Give the extent of all Babesia divergens-infected red blood cells.
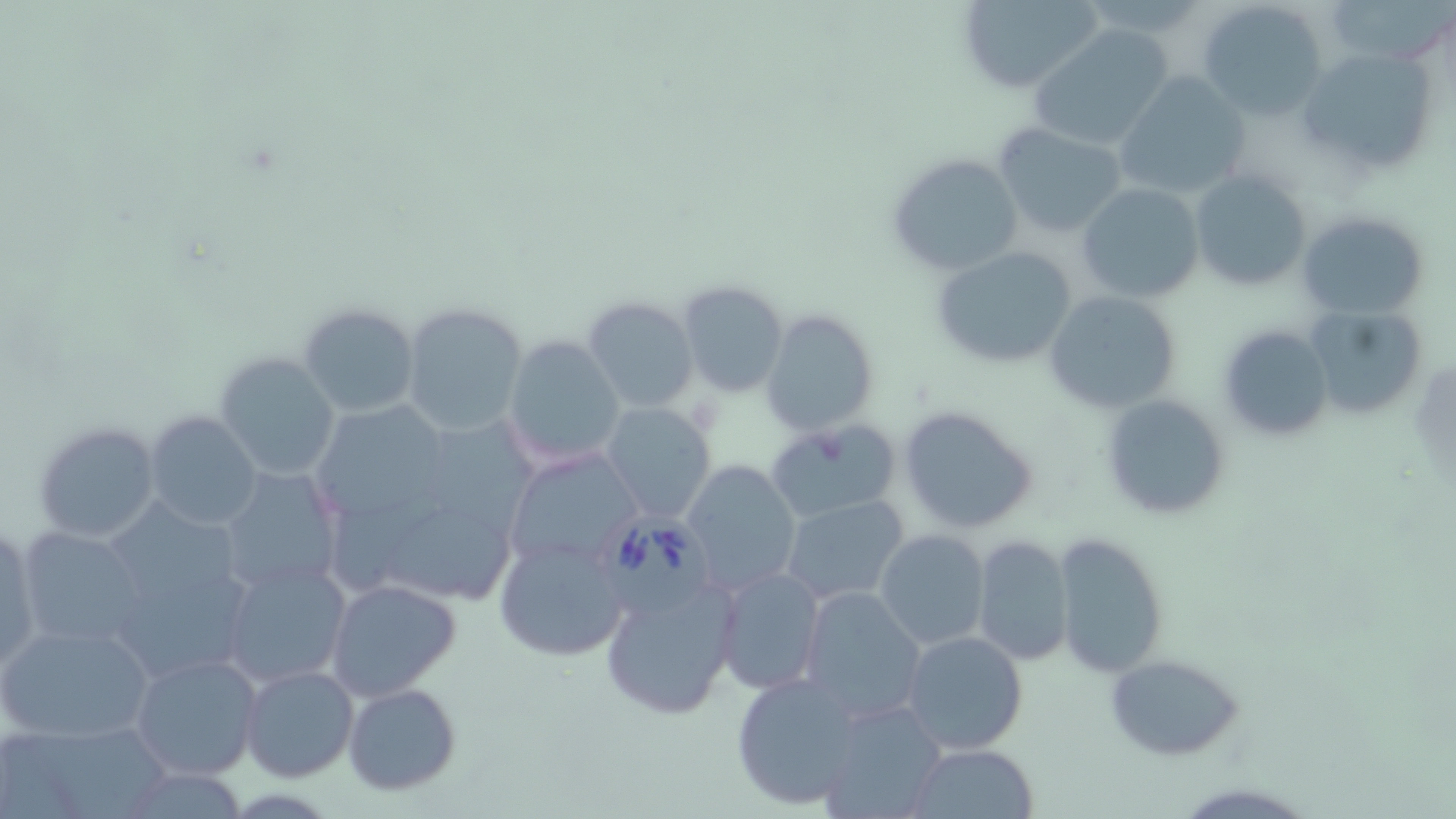
Approximate bounding boxes as [x1, y1, x2, y2] in pixels.
Babesia divergens-infected red blood cells: [604, 513, 716, 625].

Uninfected red blood cell locations: [956, 0, 1105, 94], [1328, 0, 1454, 64], [1196, 1, 1328, 120], [1027, 25, 1176, 150], [1299, 44, 1440, 176], [1113, 71, 1252, 202], [992, 121, 1130, 238], [888, 151, 1025, 275], [1191, 169, 1313, 292], [1077, 184, 1205, 302], [1298, 210, 1429, 317], [930, 244, 1077, 369], [677, 279, 789, 398], [1042, 288, 1181, 415], [581, 295, 698, 414], [400, 301, 529, 437], [295, 302, 419, 419], [1306, 305, 1429, 420], [761, 308, 879, 436], [1216, 323, 1334, 441], [504, 335, 626, 470], [215, 352, 342, 482], [1099, 393, 1230, 522], [305, 399, 456, 527], [600, 402, 717, 523], [898, 404, 1041, 535], [145, 411, 263, 530], [432, 414, 543, 531], [764, 418, 901, 524], [33, 420, 162, 544], [503, 448, 640, 572], [682, 457, 801, 595], [216, 465, 345, 597], [699, 471, 817, 681], [334, 492, 449, 597], [778, 494, 911, 606], [390, 515, 526, 607], [106, 518, 255, 689], [16, 526, 150, 655], [0, 527, 42, 674], [875, 530, 990, 650], [1051, 531, 1170, 678], [495, 535, 630, 663], [972, 535, 1074, 667], [218, 559, 352, 688], [712, 566, 827, 696], [601, 576, 738, 720], [325, 578, 460, 700], [797, 586, 925, 724], [799, 606, 1029, 741], [0, 620, 155, 745], [901, 630, 1031, 755], [130, 651, 263, 780], [1104, 653, 1246, 760], [239, 665, 360, 783], [731, 671, 862, 810], [341, 681, 463, 797], [820, 700, 946, 819], [16, 726, 178, 819], [907, 742, 1038, 818]. Slide-level diagnosis: Babesia divergens. Image is 1456×819 pixels. 1000x magnification. May-Grünwald-Giemsa stain. One field of a larger specimen. Optical microscopy. Thin blood film.